Identify the parasite.
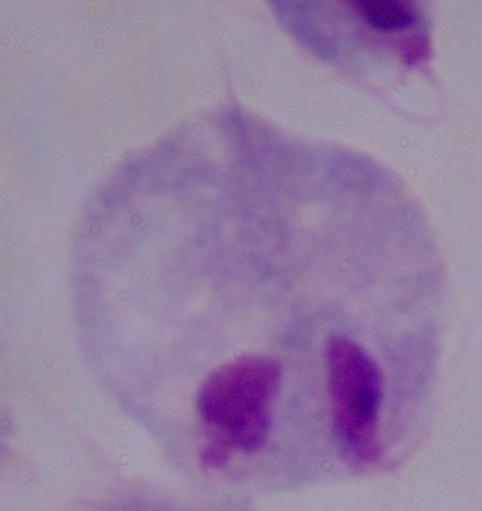

This is a trichomonad.

Captured at 1000x magnification. Photomicrograph.